Locate malaria parasites and leukocytes.
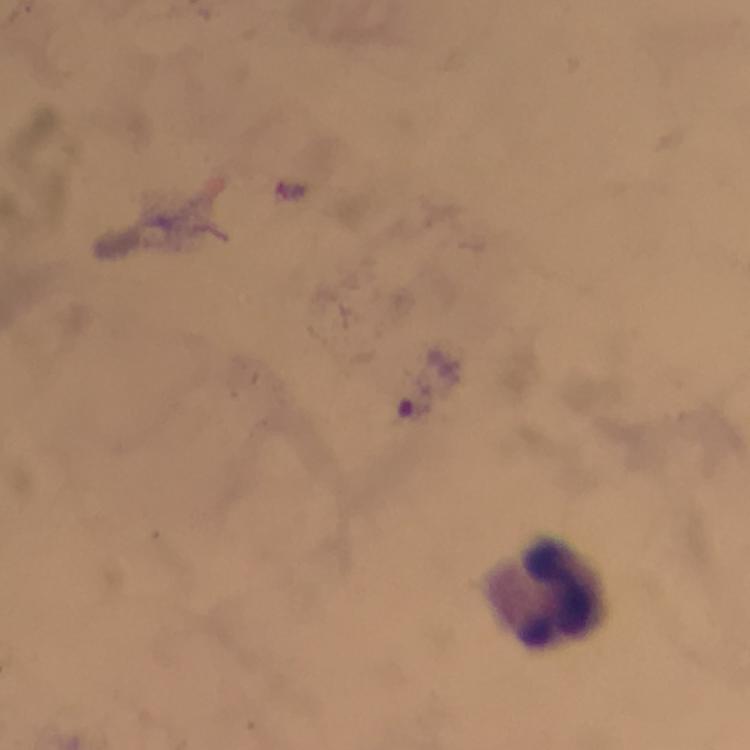
No malaria parasites seen.
Approximate object centers, in pixels from the top-left corner.
Leukocytes: (x=544, y=591).

From a malaria diagnostic workup. 100x magnification. Image is 750×750 pixels. Thick blood smear. Immersion oil applied. Giemsa stain. Photographed with a smartphone mounted on the microscope. A crop from one field of view.